Describe the morphology of the erythrocytes.
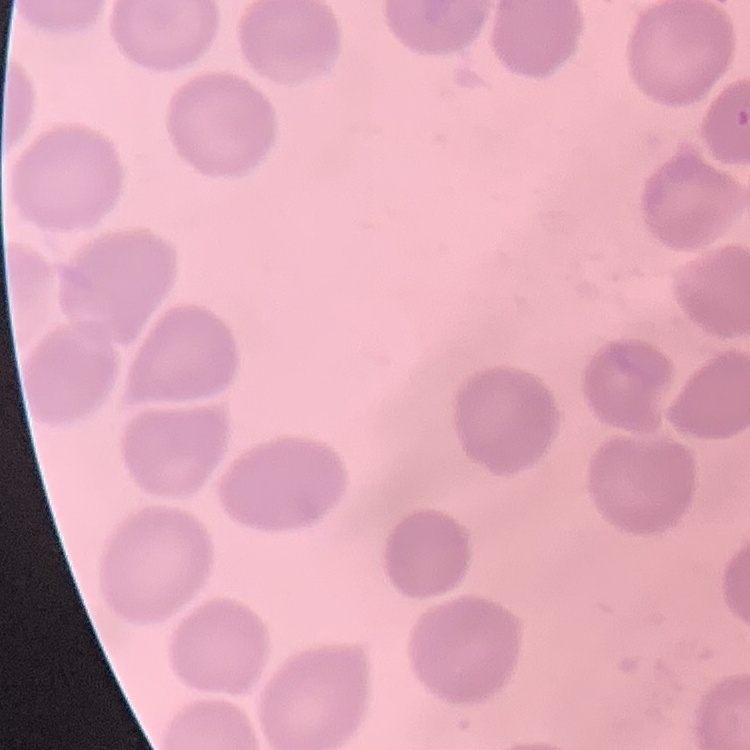

They show no rouleaux formation.

Summary:
  - Stain: Field's or Giemsa
  - Image type: one tile cut from a larger photomicrograph
  - Preparation: thin blood film